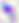

identification: Toxoplasma gondii
modality: photomicrograph
magnification: 400x